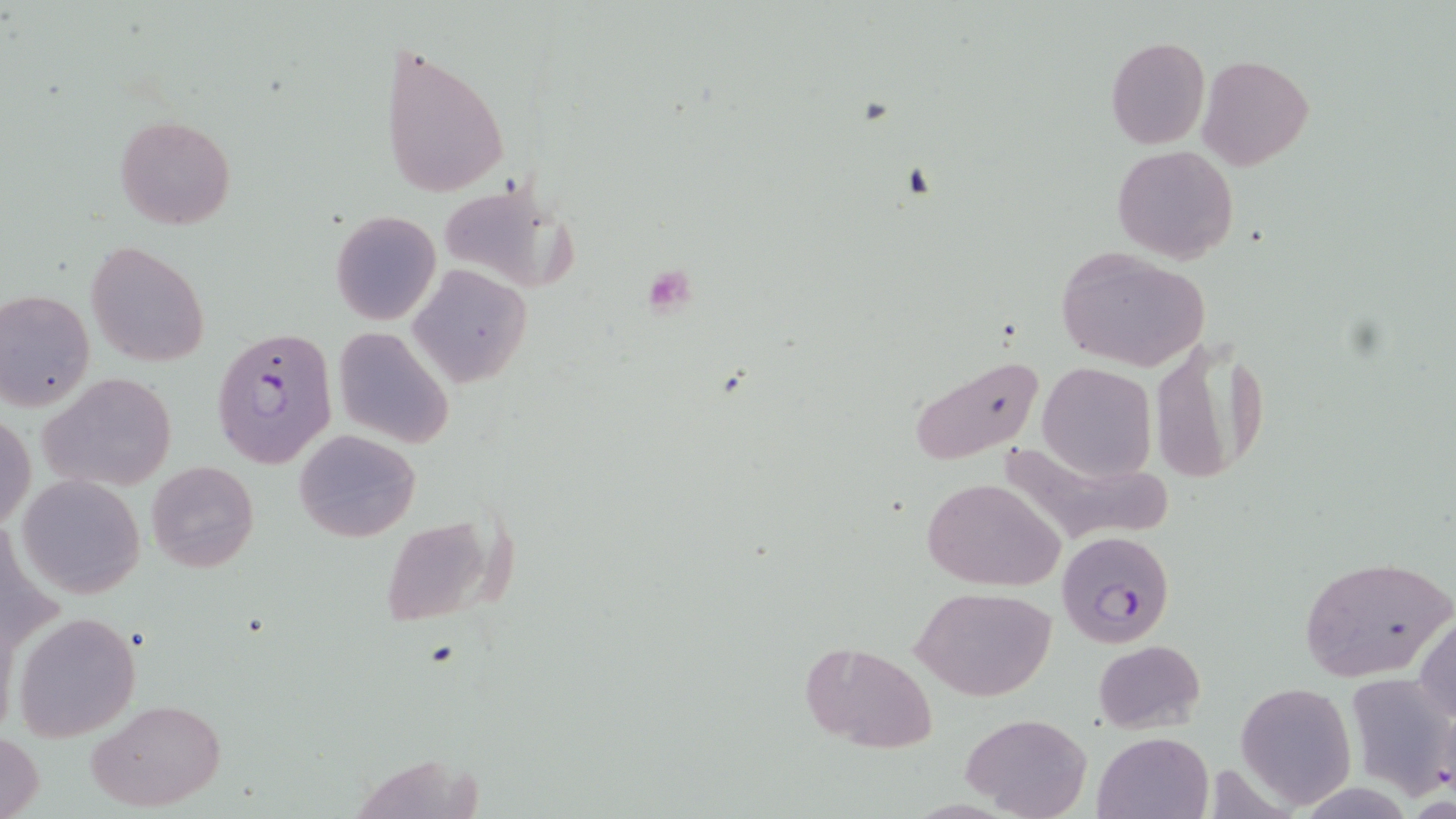

Summary:
  - Coordinate format: approximate bounding boxes as (x1, y1, x2, y2) in pixels
  - Plasmodium falciparum-infected red blood cell locations: (211, 327, 339, 471), (1057, 530, 1176, 648)
  - Platelet locations: (641, 261, 698, 315)
  - Uninfected red blood cell locations: (1105, 36, 1209, 148), (380, 39, 508, 199), (1198, 55, 1313, 170), (115, 114, 236, 228), (1111, 145, 1238, 264), (438, 185, 582, 292), (331, 210, 441, 325), (86, 241, 211, 367), (1056, 247, 1210, 373), (408, 264, 533, 388), (0, 288, 96, 411), (331, 327, 455, 449), (1152, 344, 1276, 485), (907, 357, 1043, 464), (1037, 362, 1156, 482), (38, 372, 179, 494), (1, 413, 36, 531), (294, 429, 420, 543), (146, 460, 259, 573), (16, 474, 145, 598), (921, 477, 1065, 589), (378, 515, 502, 627), (1299, 553, 1454, 686), (911, 585, 1058, 701), (1415, 609, 1456, 727), (13, 610, 141, 742), (1094, 640, 1206, 734), (797, 641, 938, 753), (1344, 672, 1456, 798), (1236, 681, 1357, 809), (88, 697, 224, 812), (962, 712, 1092, 819), (0, 731, 45, 819), (1093, 731, 1213, 819)
  - Slide-level diagnosis: Plasmodium falciparum
  - Modality: optical microscopy
  - Preparation: thin blood film
  - Field of view: single
  - Image size: 1456×819 pixels
  - Stain: May-Grünwald-Giemsa
  - Magnification: 1000x